Give the extent of all Plasmodium falciparum-infected red blood cells.
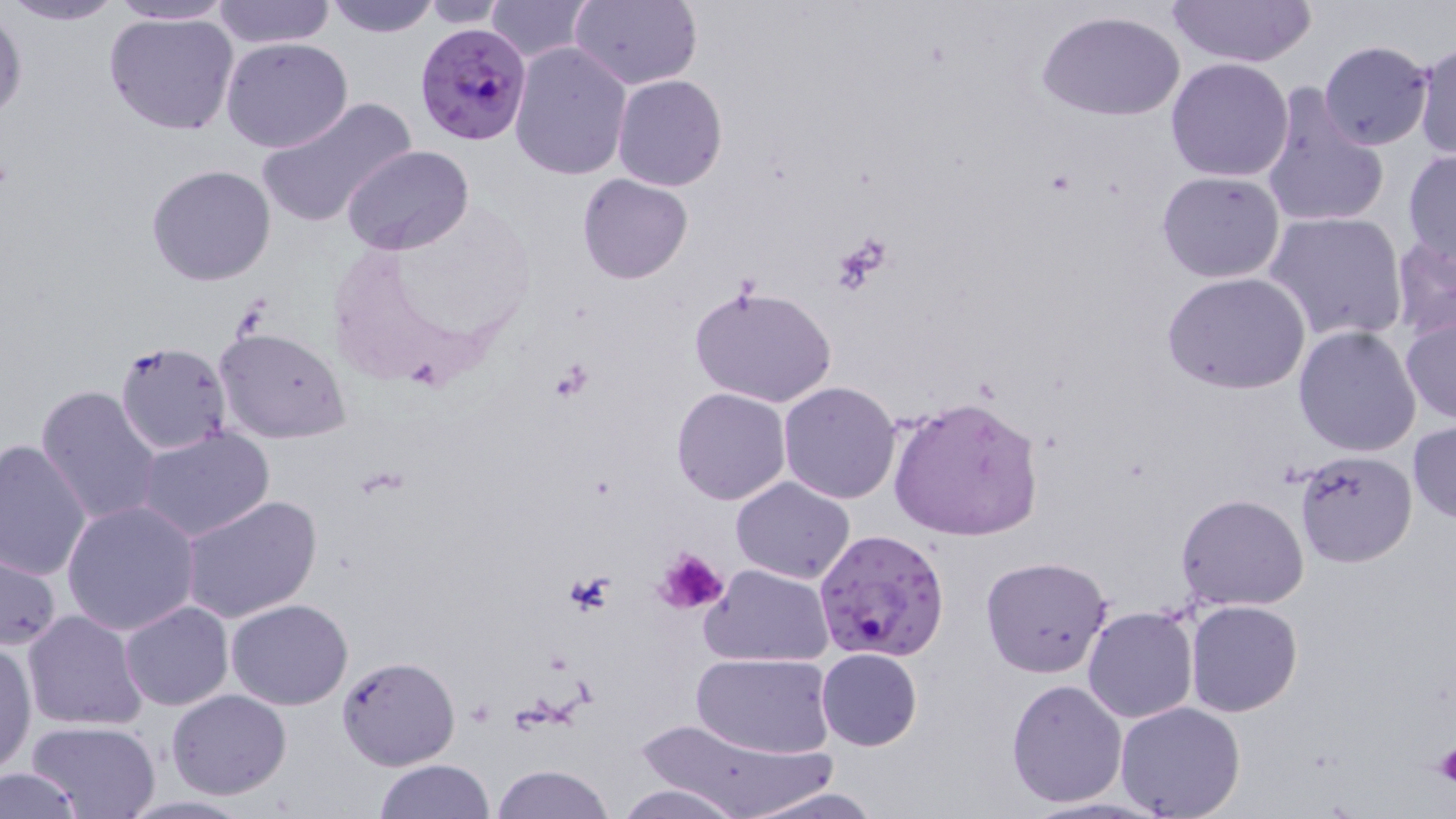

Approximate bounding boxes as (x1,y1)-(x2,y2) corner pairs in pixels.
Plasmodium falciparum-infected red blood cells: (414,20)-(533,146), (814,528)-(952,662).

Summary:
  - Uninfected red blood cell locations: (2,0)-(128,27), (107,0)-(238,25), (211,0)-(337,49), (325,0)-(438,38), (569,0)-(703,90), (1168,0)-(1316,67), (416,1)-(512,26), (484,1)-(594,62), (0,9)-(27,124), (1036,9)-(1187,122), (105,11)-(240,136), (221,38)-(352,154), (1317,40)-(1436,153), (508,41)-(632,180), (1411,41)-(1456,160), (1165,58)-(1295,182), (612,74)-(728,191), (1259,83)-(1389,232), (256,97)-(415,228), (341,145)-(475,257), (1403,148)-(1455,268), (147,163)-(276,286), (1155,171)-(1286,283), (577,173)-(693,284), (1264,210)-(1407,343), (1389,234)-(1456,343), (1162,272)-(1312,395), (689,282)-(840,408), (1400,315)-(1456,423), (1293,325)-(1422,457), (215,326)-(351,443), (114,340)-(234,456), (778,380)-(902,504), (36,385)-(162,527), (670,387)-(791,506), (887,394)-(1044,541), (1408,419)-(1456,525), (137,427)-(275,541), (1,436)-(94,581), (1293,450)-(1418,568), (731,476)-(856,584), (178,493)-(324,626), (1176,493)-(1310,610), (62,500)-(200,635), (1,550)-(62,651), (979,556)-(1113,678), (702,564)-(835,667), (225,599)-(352,711), (1185,599)-(1302,716), (120,600)-(233,711), (1082,606)-(1198,723), (22,609)-(147,731), (0,640)-(37,776), (816,647)-(922,751), (691,651)-(837,757), (335,656)-(460,771), (1006,679)-(1127,807), (167,689)-(292,799), (1115,701)-(1246,819), (632,712)-(831,819), (28,720)-(161,819), (375,759)-(496,817), (491,763)-(616,819), (0,766)-(87,817), (614,783)-(747,819), (744,785)-(885,818)
  - Platelet locations: (834,234)-(894,290), (653,547)-(728,617), (562,572)-(618,617), (1435,743)-(1456,787)
  - Slide-level diagnosis: Plasmodium falciparum
  - Modality: optical microscopy
  - Stain: May-Grünwald-Giemsa
  - Field of view: single
  - Preparation: thin blood smear
  - Image size: 1456×819 pixels
  - Magnification: 1000x